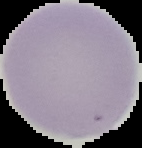

{
  "image_type": "segmented cell region on a black background",
  "preparation": "thin blood smear",
  "malaria_status": "uninfected",
  "image_size": "142×148 pixels"
}